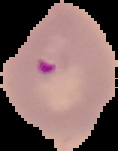
Result: malaria parasites identified. Cell region segmented out of the field of view; the surrounding area is masked to black. Image is 118×151 pixels. From a thin blood smear.